Assess this cell for malaria.
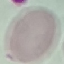

It is uninfected.

Giemsa-stained preparation. Thin smear of blood. Cell patch, automatically extracted from a larger field of view and resized to 64 × 64 pixels. Acquired by smartphone through the microscope eyepiece.